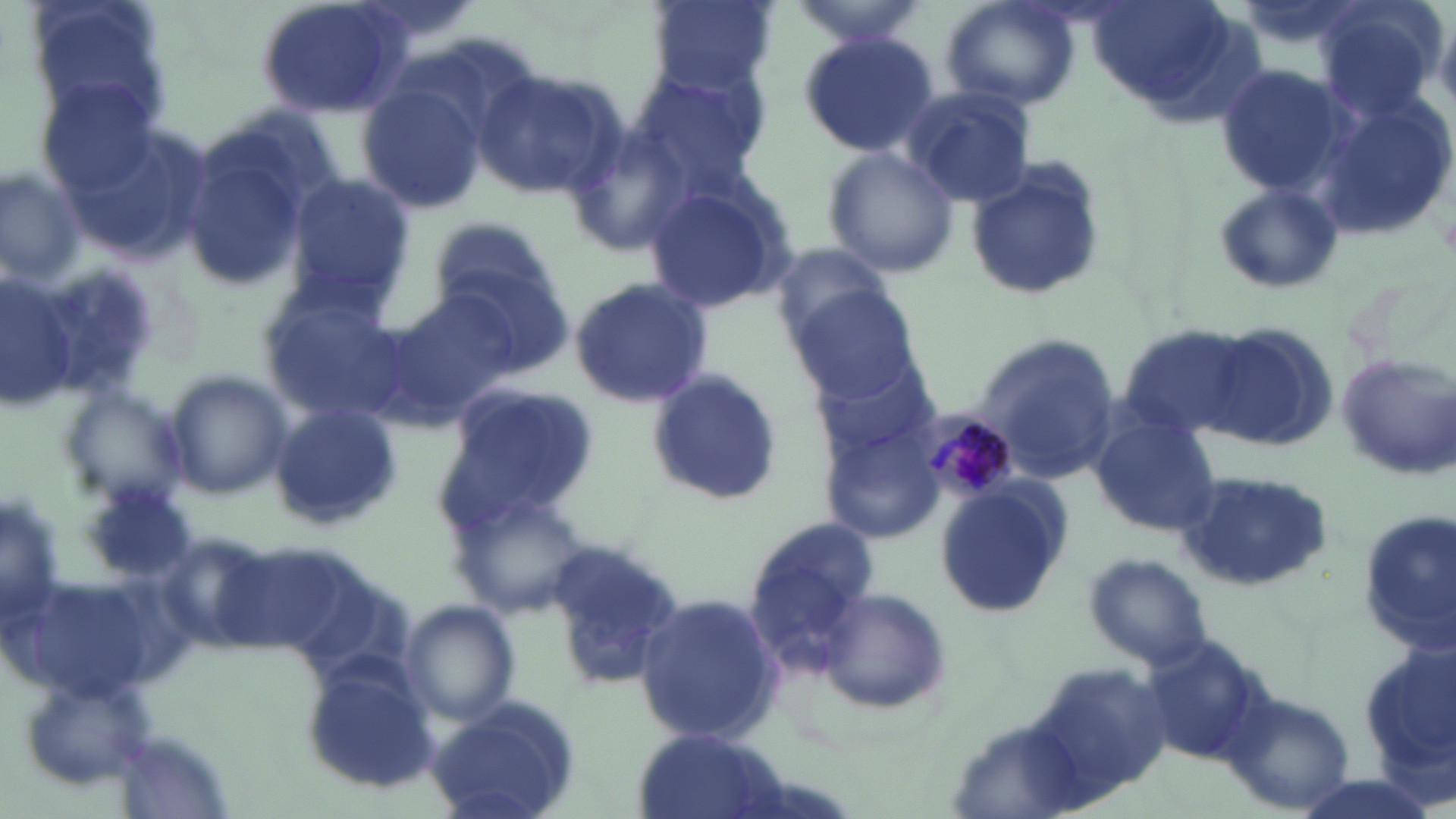 Approximate bounding boxes as [x1, y1, x2, y2] in pixels. Uninfected red blood cell locations: [25, 0, 174, 131], [255, 0, 411, 120], [789, 0, 929, 50], [939, 0, 1083, 112], [650, 1, 775, 95], [1312, 5, 1443, 121], [798, 32, 943, 159], [1215, 63, 1354, 196], [626, 68, 772, 196], [472, 69, 623, 199], [37, 76, 165, 199], [360, 84, 486, 211], [902, 86, 1035, 206], [1306, 94, 1453, 245], [561, 121, 693, 260], [175, 126, 322, 295], [821, 147, 961, 279], [964, 160, 1107, 303], [1, 166, 87, 289], [283, 174, 413, 306], [641, 179, 796, 316], [1212, 182, 1344, 295], [429, 216, 559, 319], [767, 242, 898, 347], [432, 258, 577, 384], [0, 274, 80, 410], [566, 277, 714, 408], [256, 288, 410, 425], [383, 288, 524, 421], [793, 289, 922, 401], [1119, 324, 1255, 439], [1202, 324, 1339, 452], [974, 331, 1117, 480], [809, 351, 946, 462], [1336, 354, 1455, 477], [161, 369, 292, 501], [645, 372, 783, 509], [57, 382, 192, 514], [441, 383, 597, 522], [265, 404, 403, 530], [1088, 410, 1220, 536], [822, 423, 945, 543], [1174, 472, 1334, 592], [934, 483, 1070, 618], [1, 492, 63, 631], [451, 492, 593, 616], [1354, 509, 1455, 656], [746, 513, 879, 645], [1082, 553, 1212, 670], [14, 575, 159, 702], [814, 586, 956, 716], [632, 592, 783, 747], [400, 602, 520, 727], [1355, 643, 1455, 790], [1030, 660, 1174, 800], [302, 665, 441, 792], [1220, 689, 1356, 815], [425, 698, 584, 819], [631, 729, 790, 819]. Plasmodium malariae-infected red blood cell locations: [922, 410, 1018, 500]. Slide-level diagnosis: Plasmodium malariae. Image is 1456×819 pixels. One field of a larger specimen. Thin blood film. 1000x magnification. Light microscopy. May-Grünwald-Giemsa stain.